Report the malaria status of this cell.
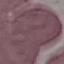
Uninfected.

Automatically extracted cell patch, resized to 64 × 64 pixels. Thin smear of blood. Photographed with a smartphone camera at the microscope eyepiece. Giemsa stain.